Classify this cell by malaria status.
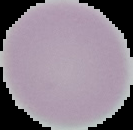
Uninfected.

Summary:
  - Image type: segmented cell region with the area outside set to black
  - Image size: 133×130 pixels
  - Preparation: thin blood film